Report the malaria status of this cell.
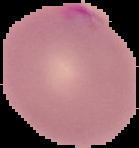
Parasitized.

From a thin blood smear. Image is 139×148 pixels. Cell region segmented out of the field of view; the surrounding area is masked to black.